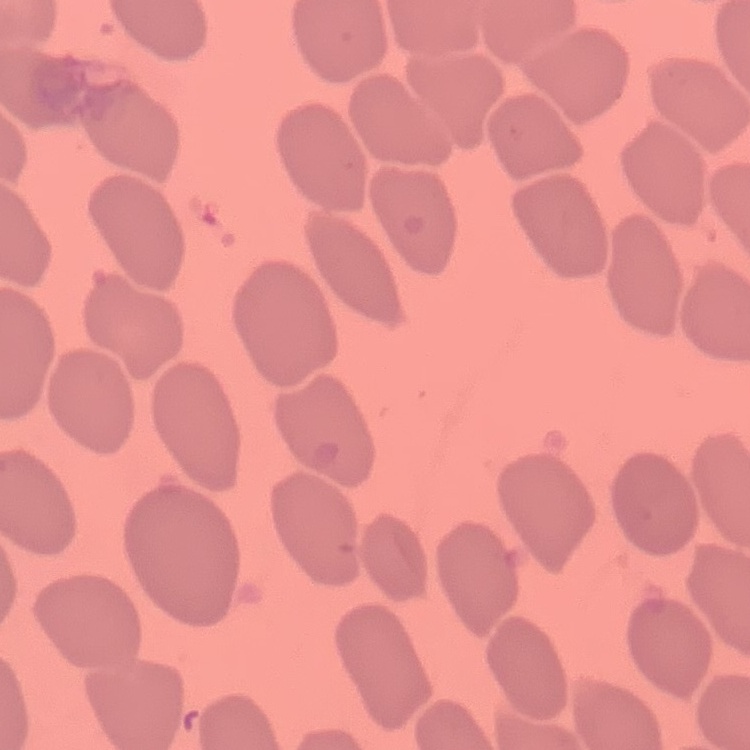
{
  "red_blood_cell_morphology": "no rouleaux formation",
  "stain": "Field's or Giemsa",
  "preparation": "thin blood film",
  "image_type": "square crop of a larger photomicrograph"
}